Locate every blood parasite and identify its species.
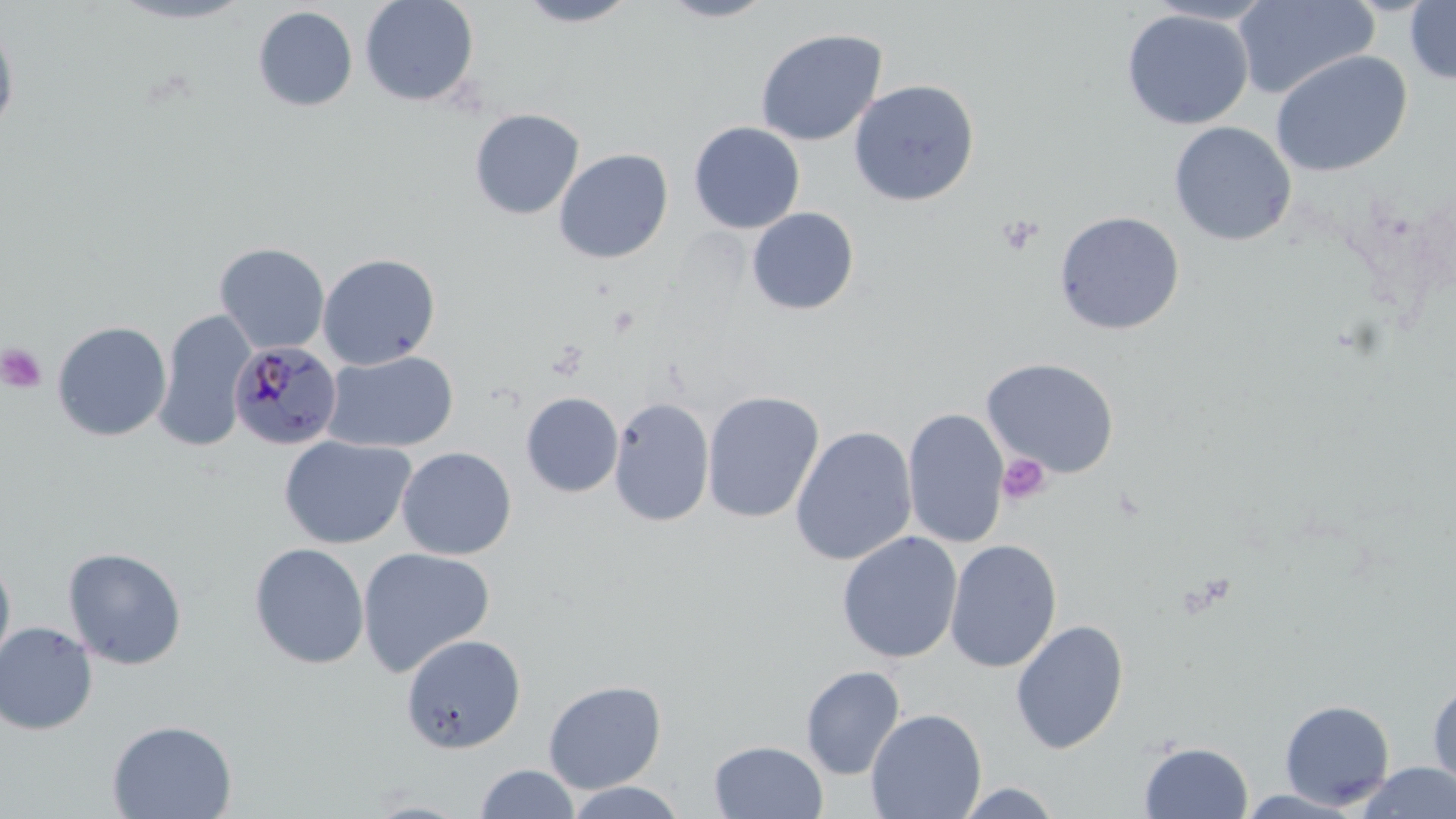

Approximate bounding boxes as [x1, y1, x2, y2] in pixels.
Plasmodium malariae-infected red blood cells: [229, 341, 343, 451].
No Plasmodium falciparum, Plasmodium ovale, Plasmodium vivax, Babesia divergens, or Trypanosoma brucei observed.

Summary:
  - Uninfected red blood cell locations: [108, 0, 257, 25], [359, 0, 480, 107], [515, 0, 642, 28], [656, 0, 778, 23], [1233, 0, 1379, 100], [1404, 0, 1456, 85], [253, 6, 358, 111], [1121, 9, 1253, 129], [0, 17, 19, 141], [755, 28, 887, 146], [1271, 50, 1412, 177], [848, 79, 980, 206], [469, 108, 584, 220], [688, 121, 805, 234], [1169, 121, 1296, 246], [553, 148, 674, 264], [747, 207, 859, 315], [1053, 210, 1185, 335], [214, 242, 330, 354], [317, 253, 440, 370], [153, 309, 254, 452], [51, 320, 172, 442], [323, 350, 459, 453], [981, 357, 1120, 478], [702, 390, 824, 524], [521, 392, 623, 497], [608, 397, 714, 527], [902, 407, 1009, 549], [790, 426, 917, 566], [278, 435, 416, 550], [396, 446, 517, 560], [836, 531, 963, 664], [944, 539, 1063, 673], [249, 542, 370, 670], [63, 547, 187, 670], [356, 547, 495, 677], [0, 554, 16, 679], [1010, 619, 1130, 755], [0, 622, 98, 735], [400, 633, 526, 754], [801, 666, 905, 780], [543, 679, 666, 794], [1427, 679, 1456, 795], [1279, 699, 1395, 810], [866, 708, 987, 819], [107, 718, 237, 818], [709, 740, 829, 819], [1139, 741, 1253, 818], [1355, 762, 1456, 818], [474, 764, 581, 818], [564, 781, 686, 818], [955, 782, 1064, 817], [1236, 788, 1365, 818]
  - Platelet locations: [998, 216, 1043, 256], [0, 344, 47, 394], [997, 453, 1051, 506]
  - Slide-level diagnosis: Plasmodium malariae
  - Modality: light microscopy
  - Image size: 1456×819 pixels
  - Magnification: 1000x
  - Preparation: thin blood smear
  - Field of view: one of a larger specimen
  - Stain: May-Grünwald-Giemsa